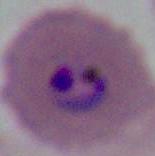

Summary:
  - Identification: Plasmodium
  - Modality: photomicrograph
  - Magnification: 400x or 1000x